Identify the parasite.
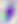
Toxoplasma gondii.

Summary:
  - Modality: photomicrograph
  - Magnification: 400x